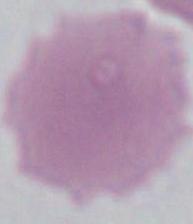 An erythrocyte is shown. Photomicrograph. Captured at 1000x magnification.